State which parasite is depicted.
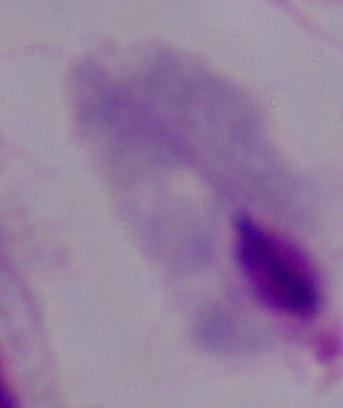

A trichomonad.

Summary:
  - Magnification: 1000x
  - Modality: photomicrograph